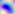
magnification = 400x
modality = micrograph
identification = Toxoplasma gondii